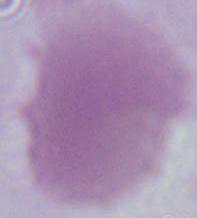

Summary:
  - Identification: erythrocyte
  - Magnification: 1000x
  - Modality: photomicrograph